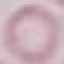 Result: negative for malaria parasites. Giemsa-stained preparation. Automatically extracted cell patch, resized to 64 × 64 pixels. Acquired by smartphone through the microscope eyepiece. Thin blood film.